Report the malaria status of this cell.
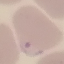
Parasitized.

Summary:
  - Capture: smartphone through the microscope eyepiece
  - Image type: cell patch, automatically extracted from a larger field of view and resized to 64 × 64 pixels
  - Preparation: thin blood smear
  - Stain: Giemsa